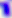 Toxoplasma gondii is seen. 400x magnification. Micrograph.